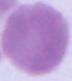

identification: red blood cell
magnification: 1000x
modality: photomicrograph